Locate and identify every blood parasite.
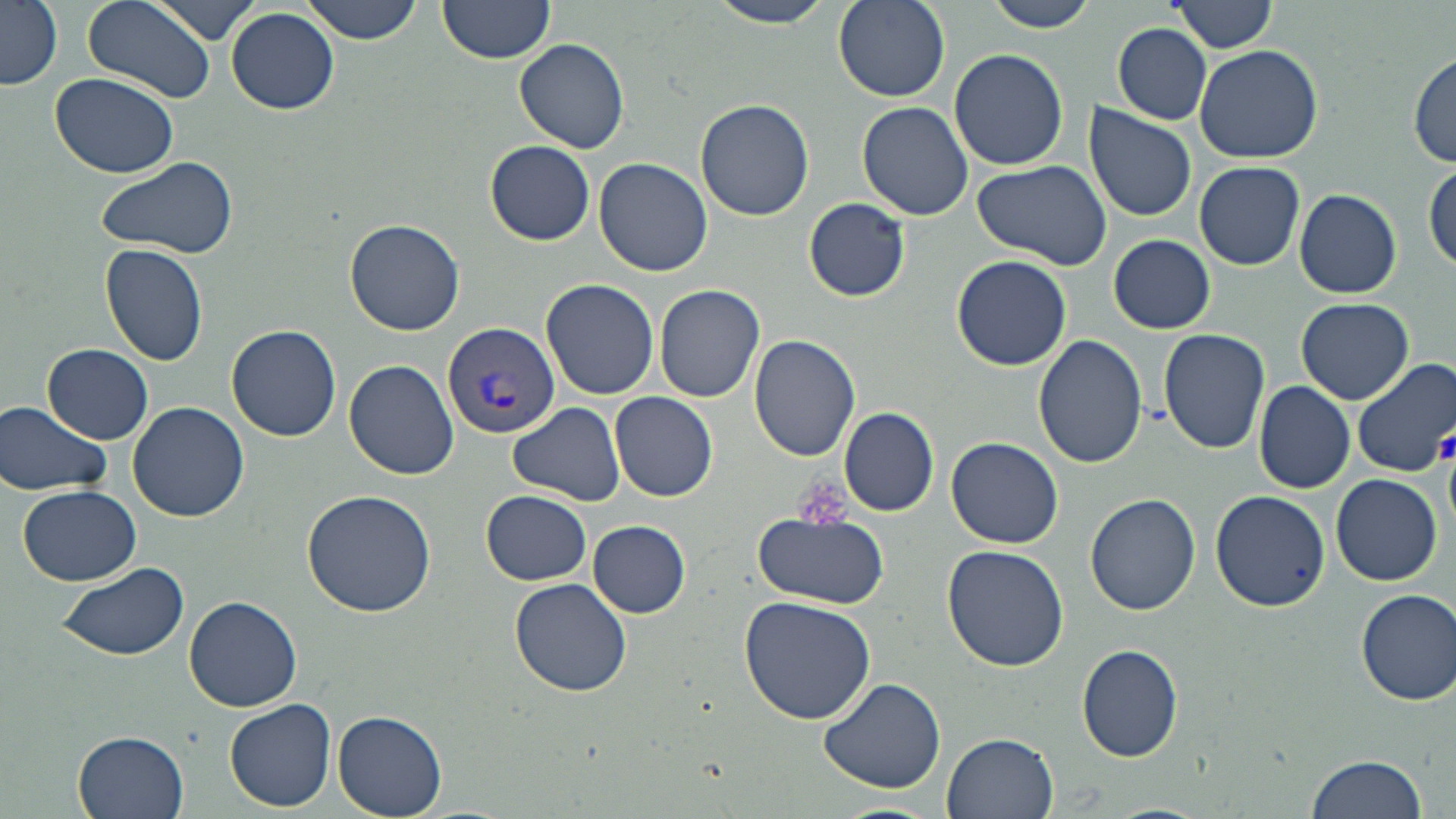
Approximate bounding boxes as named x1/y1/x2/y2 corners in pixels.
Plasmodium vivax-infected red blood cells: (x1=443, y1=323, x2=559, y2=439).
No Plasmodium falciparum, Plasmodium ovale, Plasmodium malariae, Babesia divergens, or Trypanosoma brucei observed.

Summary:
  - Platelet locations: (x1=1437, y1=431, x2=1456, y2=466), (x1=792, y1=475, x2=851, y2=531)
  - Uninfected red blood cell locations: (x1=0, y1=0, x2=62, y2=90), (x1=82, y1=0, x2=219, y2=105), (x1=151, y1=0, x2=263, y2=43), (x1=302, y1=0, x2=423, y2=45), (x1=438, y1=0, x2=557, y2=67), (x1=710, y1=0, x2=838, y2=31), (x1=833, y1=0, x2=950, y2=103), (x1=982, y1=0, x2=1101, y2=32), (x1=1170, y1=0, x2=1279, y2=54), (x1=227, y1=8, x2=339, y2=114), (x1=1113, y1=24, x2=1213, y2=124), (x1=516, y1=35, x2=630, y2=155), (x1=1194, y1=44, x2=1323, y2=165), (x1=949, y1=48, x2=1069, y2=171), (x1=1411, y1=51, x2=1455, y2=169), (x1=51, y1=73, x2=180, y2=179), (x1=696, y1=99, x2=815, y2=221), (x1=856, y1=101, x2=974, y2=221), (x1=1084, y1=103, x2=1198, y2=222), (x1=485, y1=140, x2=595, y2=244), (x1=97, y1=155, x2=238, y2=260), (x1=593, y1=157, x2=713, y2=277), (x1=971, y1=158, x2=1113, y2=272), (x1=1427, y1=160, x2=1456, y2=273), (x1=1195, y1=161, x2=1305, y2=269), (x1=1294, y1=187, x2=1401, y2=298), (x1=804, y1=198, x2=911, y2=302), (x1=344, y1=219, x2=465, y2=335), (x1=1110, y1=235, x2=1214, y2=333), (x1=99, y1=244, x2=210, y2=369), (x1=952, y1=255, x2=1071, y2=368), (x1=541, y1=278, x2=659, y2=399), (x1=654, y1=283, x2=768, y2=402), (x1=1297, y1=296, x2=1414, y2=404), (x1=227, y1=324, x2=342, y2=442), (x1=1156, y1=328, x2=1271, y2=455), (x1=748, y1=334, x2=861, y2=461), (x1=1034, y1=334, x2=1148, y2=470), (x1=43, y1=343, x2=153, y2=444), (x1=1350, y1=357, x2=1456, y2=479), (x1=346, y1=360, x2=459, y2=480), (x1=1251, y1=380, x2=1355, y2=494), (x1=610, y1=392, x2=718, y2=503), (x1=1, y1=400, x2=114, y2=496), (x1=127, y1=400, x2=250, y2=522), (x1=507, y1=402, x2=626, y2=505), (x1=838, y1=405, x2=938, y2=516), (x1=946, y1=435, x2=1065, y2=548), (x1=1331, y1=474, x2=1442, y2=587), (x1=17, y1=483, x2=144, y2=584), (x1=1209, y1=488, x2=1330, y2=611), (x1=301, y1=490, x2=437, y2=616), (x1=482, y1=490, x2=591, y2=584), (x1=1084, y1=494, x2=1200, y2=616), (x1=753, y1=510, x2=889, y2=608), (x1=589, y1=520, x2=690, y2=618), (x1=942, y1=544, x2=1069, y2=671), (x1=56, y1=562, x2=191, y2=660), (x1=510, y1=577, x2=633, y2=697), (x1=1355, y1=589, x2=1456, y2=705), (x1=739, y1=593, x2=879, y2=725), (x1=186, y1=595, x2=302, y2=712), (x1=1075, y1=643, x2=1185, y2=763), (x1=816, y1=677, x2=947, y2=793), (x1=224, y1=698, x2=337, y2=811), (x1=334, y1=712, x2=447, y2=816), (x1=73, y1=729, x2=189, y2=819), (x1=943, y1=731, x2=1058, y2=817), (x1=1304, y1=751, x2=1430, y2=819), (x1=1101, y1=803, x2=1215, y2=819)
  - Slide-level diagnosis: Plasmodium vivax
  - Modality: optical microscopy
  - Magnification: 1000x
  - Stain: May-Grünwald-Giemsa
  - Field of view: one of a larger specimen
  - Image size: 1456×819 pixels
  - Preparation: thin blood smear